Report the malaria status of this cell.
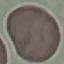

It is uninfected.

Summary:
  - Capture: smartphone through the microscope eyepiece
  - Image type: cell patch, automatically extracted from a larger field of view and resized to 64 × 64 pixels
  - Stain: Giemsa
  - Preparation: thin blood smear